Report the malaria status of this cell.
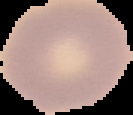
Uninfected.

Summary:
  - Image size: 133×115 pixels
  - Image type: segmented cell region with the area outside set to black
  - Preparation: thin blood smear